Assess this cell for malaria.
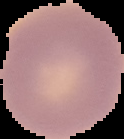
Uninfected.

Summary:
  - Preparation: thin blood film
  - Image size: 124×139 pixels
  - Image type: cell region segmented out of the field of view; surrounding area masked to black